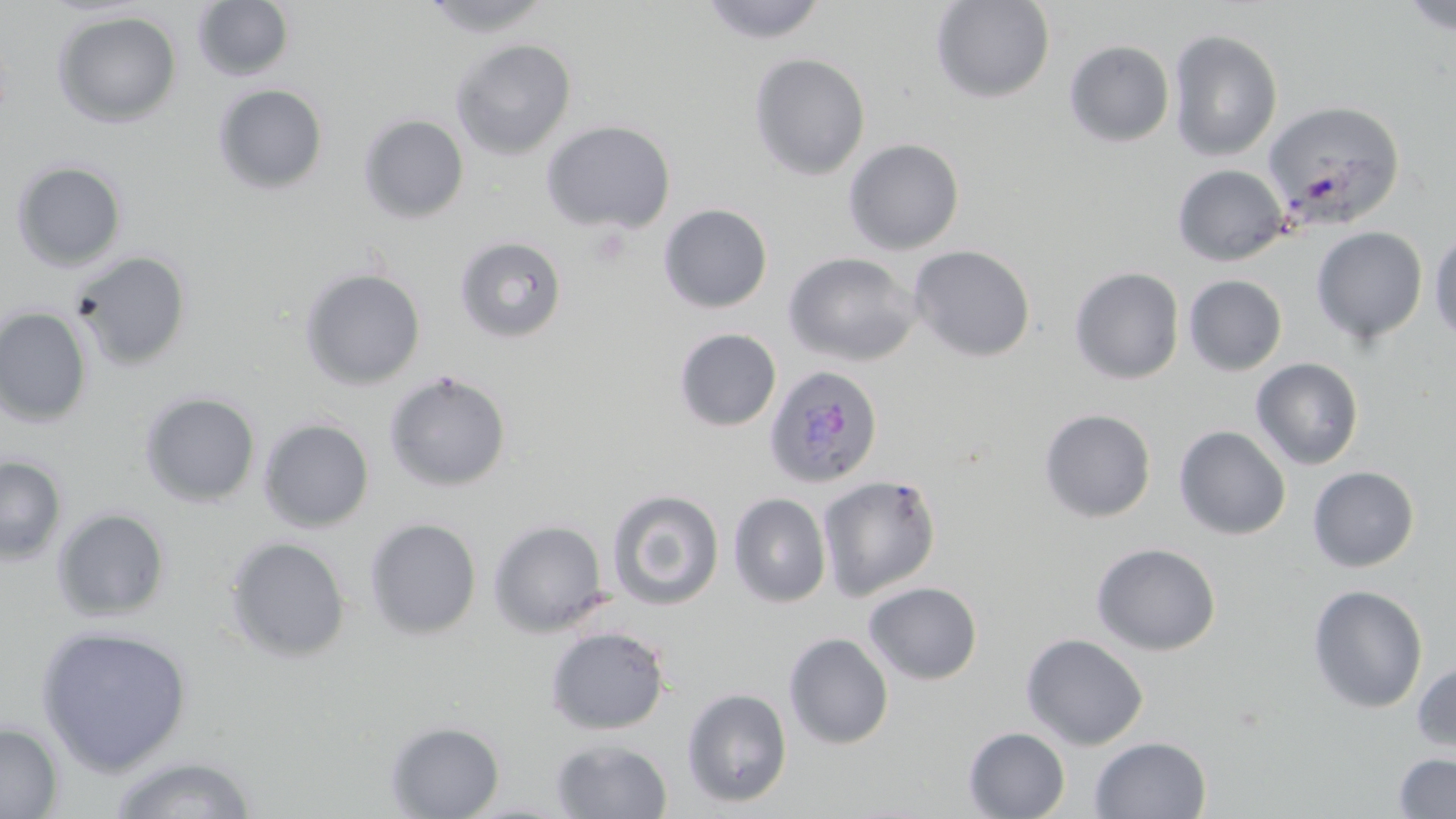

Summary:
  - Coordinate format: approximate bounding boxes as (x1, y1, x2, y2) in pixels
  - Plasmodium ovale-infected red blood cell locations: (763, 364, 883, 488)
  - Uninfected red blood cell locations: (192, 0, 294, 82), (420, 0, 554, 38), (698, 0, 828, 44), (929, 0, 1055, 104), (1399, 0, 1456, 36), (53, 10, 182, 128), (1168, 29, 1283, 162), (450, 38, 576, 159), (1064, 40, 1175, 147), (748, 53, 871, 180), (213, 84, 329, 195), (1263, 101, 1408, 230), (359, 115, 469, 223), (541, 120, 676, 234), (843, 138, 965, 255), (11, 160, 127, 272), (1172, 164, 1289, 266), (658, 204, 773, 313), (1311, 227, 1428, 344), (1428, 227, 1456, 347), (454, 236, 568, 343), (908, 245, 1036, 362), (69, 250, 192, 372), (782, 252, 921, 367), (1069, 267, 1184, 385), (299, 268, 426, 390), (1183, 275, 1287, 376), (0, 306, 93, 428), (674, 328, 781, 431), (1251, 358, 1364, 470), (383, 371, 512, 493), (139, 391, 261, 508), (1039, 408, 1156, 523), (258, 418, 374, 533), (1173, 425, 1291, 540), (0, 455, 68, 565), (1307, 466, 1420, 572), (817, 474, 941, 601), (606, 488, 725, 611), (728, 492, 832, 608), (52, 507, 171, 622), (364, 518, 482, 640), (488, 519, 609, 637), (224, 536, 350, 662), (1091, 542, 1222, 656), (863, 581, 983, 685), (1307, 585, 1428, 713), (35, 624, 192, 775), (545, 626, 670, 735), (783, 632, 894, 750), (1021, 633, 1149, 751), (1413, 657, 1456, 756), (682, 687, 793, 808), (385, 721, 505, 818), (0, 722, 63, 818), (963, 726, 1070, 818), (1089, 736, 1212, 819), (550, 739, 673, 818), (107, 753, 260, 819), (1393, 753, 1456, 817)
  - Slide-level diagnosis: Plasmodium ovale
  - Preparation: thin blood smear
  - Field of view: single
  - Image size: 1456×819 pixels
  - Magnification: 1000x
  - Stain: May-Grünwald-Giemsa
  - Modality: optical microscopy